Locate and identify every blood parasite.
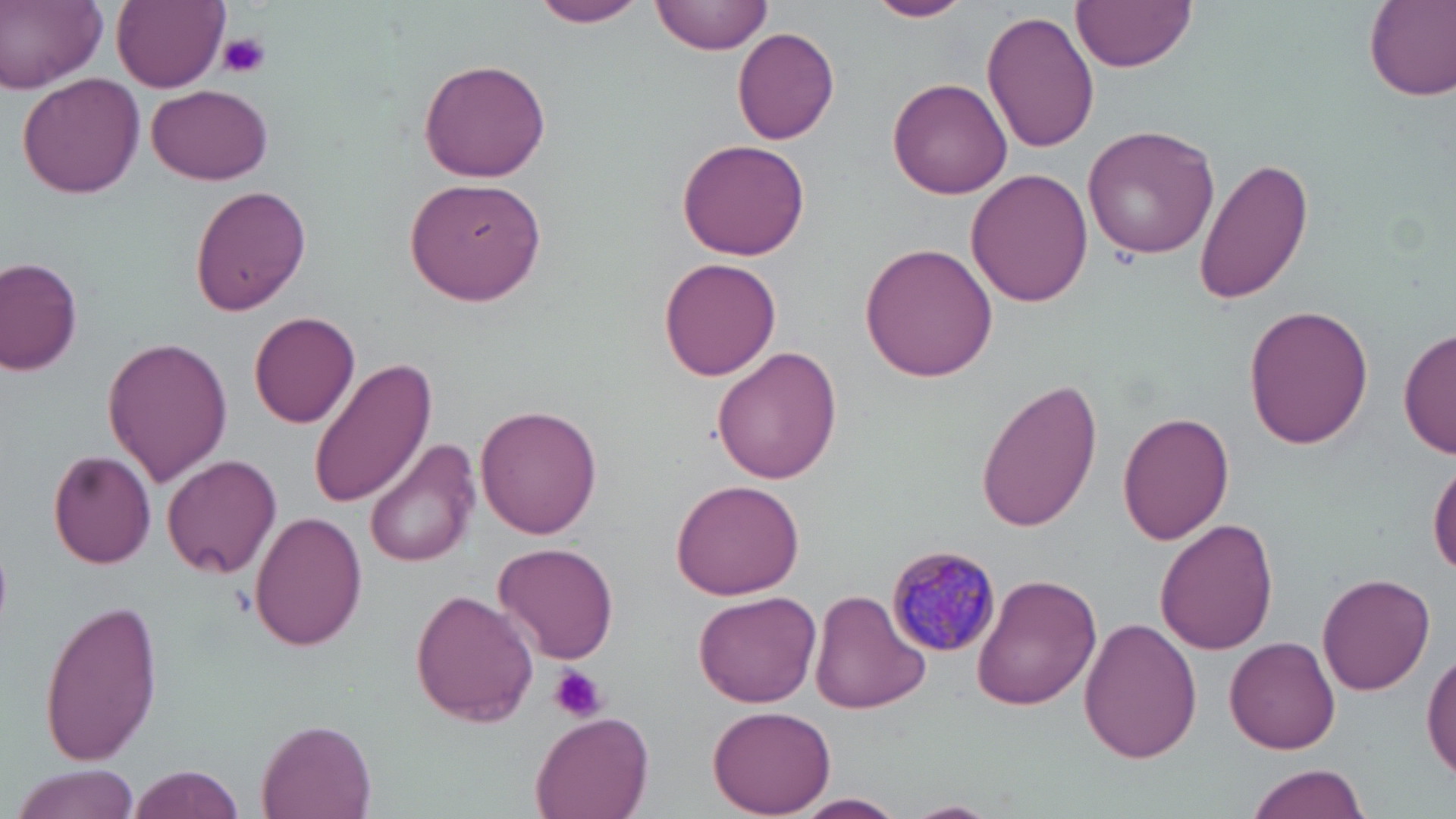

Approximate bounding boxes as (x1, y1, x2, y2) in pixels.
Plasmodium malariae-infected red blood cells: (885, 544, 1003, 659).
No Plasmodium falciparum, Plasmodium ovale, Plasmodium vivax, Babesia divergens, or Trypanosoma brucei observed.

Platelet locations: (219, 31, 271, 78), (549, 665, 605, 723). Uninfected red blood cell locations: (2, 0, 108, 92), (112, 0, 228, 90), (652, 0, 770, 56), (864, 0, 973, 23), (1073, 0, 1197, 72), (1363, 0, 1456, 101), (529, 2, 649, 30), (982, 10, 1100, 154), (733, 26, 841, 144), (417, 57, 551, 182), (17, 72, 145, 197), (887, 77, 1013, 200), (147, 83, 275, 182), (1083, 125, 1220, 258), (676, 137, 809, 260), (1195, 158, 1314, 306), (965, 169, 1093, 305), (404, 175, 550, 307), (191, 185, 311, 316), (859, 243, 997, 381), (1, 257, 83, 375), (659, 257, 781, 381), (1244, 305, 1372, 448), (247, 312, 361, 427), (1398, 327, 1455, 460), (103, 337, 233, 488), (712, 346, 843, 485), (308, 356, 435, 507), (977, 379, 1104, 533), (475, 405, 602, 538), (1117, 409, 1235, 544), (364, 439, 481, 570), (47, 449, 155, 568), (161, 455, 282, 579), (1429, 457, 1456, 583), (672, 480, 806, 602), (250, 511, 365, 651), (1154, 517, 1276, 655), (493, 540, 619, 666), (972, 572, 1101, 711), (1318, 572, 1435, 695), (411, 590, 538, 727), (692, 591, 823, 710), (810, 591, 928, 714), (39, 595, 164, 764), (1077, 616, 1201, 765), (1226, 635, 1340, 754), (1422, 643, 1456, 782), (709, 706, 835, 817), (530, 709, 654, 819), (257, 719, 378, 819), (9, 764, 143, 819), (1245, 765, 1371, 819), (132, 766, 246, 819), (792, 792, 910, 818). Slide-level diagnosis: Plasmodium malariae. One field of a larger specimen. May-Grünwald-Giemsa stain. 1000x magnification. Thin blood smear. Light microscopy. Image is 1456×819 pixels.